Give the extent of all Trypanosoma brucei.
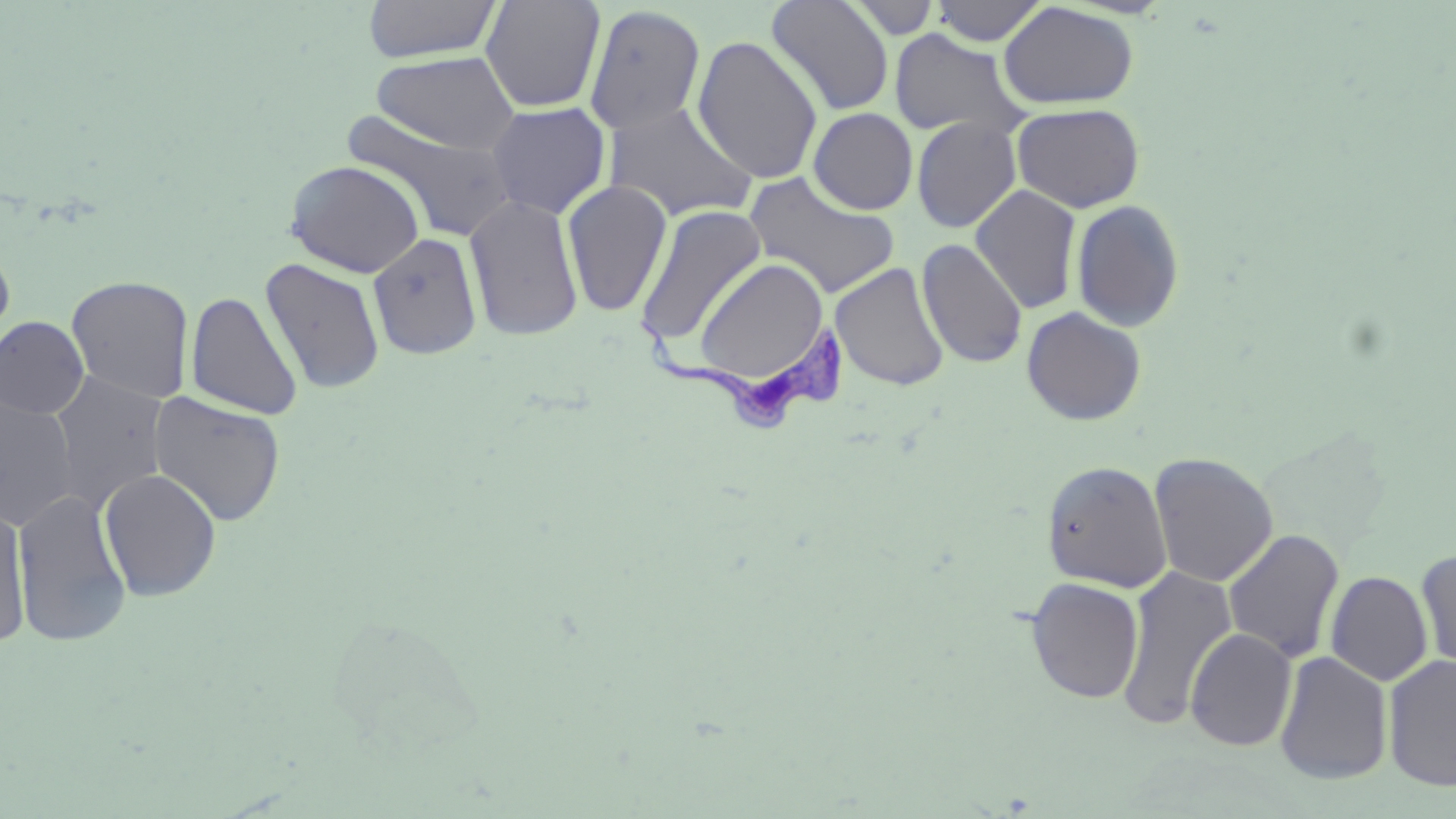

Approximate bounding boxes as named x1/y1/x2/y2 corners in pixels.
Trypanosoma brucei: (x1=636, y1=312, x2=852, y2=432).

Summary:
  - Uninfected red blood cell locations: (x1=362, y1=0, x2=503, y2=63), (x1=480, y1=0, x2=606, y2=113), (x1=845, y1=0, x2=943, y2=39), (x1=765, y1=1, x2=895, y2=117), (x1=929, y1=1, x2=1049, y2=46), (x1=998, y1=2, x2=1139, y2=109), (x1=583, y1=4, x2=706, y2=135), (x1=888, y1=29, x2=1031, y2=140), (x1=692, y1=34, x2=824, y2=185), (x1=370, y1=50, x2=522, y2=155), (x1=486, y1=101, x2=611, y2=219), (x1=602, y1=101, x2=758, y2=222), (x1=1012, y1=103, x2=1145, y2=213), (x1=808, y1=107, x2=918, y2=215), (x1=344, y1=111, x2=520, y2=243), (x1=911, y1=117, x2=1022, y2=233), (x1=285, y1=159, x2=425, y2=278), (x1=742, y1=170, x2=901, y2=299), (x1=561, y1=179, x2=673, y2=318), (x1=970, y1=184, x2=1082, y2=314), (x1=464, y1=192, x2=584, y2=341), (x1=1070, y1=198, x2=1185, y2=332), (x1=635, y1=203, x2=768, y2=348), (x1=368, y1=231, x2=484, y2=360), (x1=0, y1=236, x2=17, y2=355), (x1=916, y1=238, x2=1028, y2=369), (x1=259, y1=257, x2=386, y2=395), (x1=693, y1=257, x2=831, y2=388), (x1=830, y1=262, x2=950, y2=392), (x1=66, y1=275, x2=194, y2=404), (x1=185, y1=290, x2=303, y2=420), (x1=1021, y1=306, x2=1147, y2=425), (x1=0, y1=316, x2=90, y2=419), (x1=47, y1=370, x2=170, y2=511), (x1=148, y1=391, x2=286, y2=527), (x1=0, y1=393, x2=79, y2=531), (x1=1148, y1=452, x2=1279, y2=588), (x1=1041, y1=460, x2=1173, y2=592), (x1=98, y1=468, x2=221, y2=601), (x1=12, y1=488, x2=132, y2=647), (x1=0, y1=500, x2=32, y2=649), (x1=1222, y1=528, x2=1345, y2=664), (x1=1415, y1=548, x2=1456, y2=675), (x1=1117, y1=565, x2=1237, y2=732), (x1=1326, y1=570, x2=1433, y2=686), (x1=1025, y1=577, x2=1145, y2=704), (x1=1185, y1=627, x2=1297, y2=751), (x1=1274, y1=650, x2=1393, y2=785), (x1=1383, y1=654, x2=1456, y2=791)
  - Slide-level diagnosis: Trypanosoma brucei
  - Modality: light microscopy
  - Preparation: thin blood film
  - Magnification: 1000x
  - Field of view: one of a larger specimen
  - Stain: May-Grünwald-Giemsa
  - Image size: 1456×819 pixels